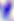
magnification = 400x
modality = micrograph
identification = Toxoplasma gondii